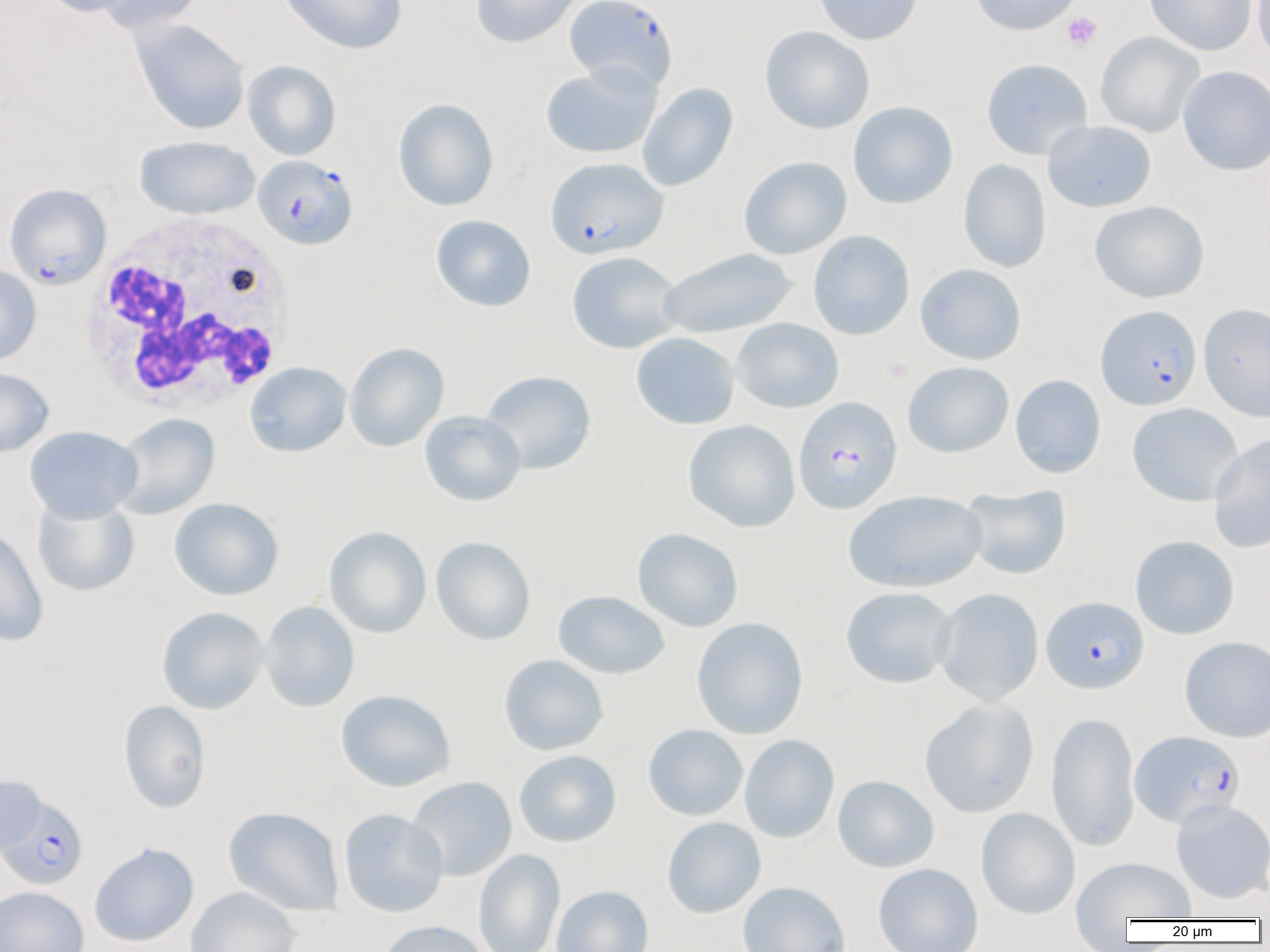

{
  "slide_level_diagnosis": "Plasmodium falciparum",
  "preparation": "thin blood smear",
  "platelet_locations": "approximate bounding boxes as (x1, y1, x2, y2) in pixels: (1063, 12, 1102, 50)",
  "modality": "optical microscopy",
  "white_blood_cell_locations": "approximate bounding boxes as (x1, y1, x2, y2) in pixels: (80, 213, 298, 416)",
  "plasmodium_falciparum_infected_red_blood_cell_locations": "approximate bounding boxes as (x1, y1, x2, y2) in pixels: (565, 0, 677, 92), (253, 155, 357, 249), (545, 157, 668, 259), (4, 183, 111, 290), (1096, 305, 1201, 410), (793, 396, 901, 515), (1041, 596, 1149, 694), (1130, 730, 1244, 828), (0, 794, 89, 890)",
  "image_size": "1270×952 pixels",
  "uninfected_red_blood_cell_locations": "approximate bounding boxes as (x1, y1, x2, y2) in pixels: (43, 0, 142, 18), (94, 0, 205, 35), (278, 0, 407, 55), (469, 0, 585, 49), (813, 0, 923, 45), (968, 0, 1083, 36), (1144, 0, 1257, 55), (1252, 0, 1270, 68), (129, 19, 250, 135), (760, 26, 874, 134), (1095, 31, 1204, 138), (981, 58, 1093, 160), (242, 60, 341, 160), (540, 63, 661, 159), (1178, 65, 1270, 176), (637, 82, 738, 192), (392, 98, 499, 211), (848, 101, 958, 209), (1043, 120, 1157, 212), (133, 135, 260, 220), (738, 155, 852, 259), (958, 159, 1052, 273), (1090, 200, 1210, 303), (430, 214, 536, 312), (808, 230, 915, 340), (658, 248, 797, 338), (566, 251, 684, 354), (915, 263, 1026, 365), (0, 264, 42, 366), (1198, 302, 1270, 421), (732, 318, 844, 413), (631, 332, 740, 429), (344, 341, 449, 452), (902, 361, 1014, 458), (245, 362, 351, 457), (0, 367, 54, 458), (480, 370, 596, 474), (1010, 375, 1106, 478), (1127, 402, 1243, 506), (419, 410, 526, 506), (112, 413, 219, 519), (683, 419, 801, 532), (25, 425, 143, 523), (1208, 433, 1270, 554), (960, 484, 1072, 580), (844, 490, 986, 593), (32, 495, 139, 597), (169, 497, 284, 600), (0, 521, 48, 647), (323, 526, 432, 639), (632, 527, 744, 632), (1130, 535, 1239, 639), (431, 536, 535, 646), (840, 586, 957, 689), (933, 588, 1044, 706), (553, 590, 669, 679), (259, 601, 360, 712), (156, 606, 269, 714), (691, 617, 808, 740), (1180, 635, 1270, 743), (498, 654, 609, 756), (335, 689, 456, 792), (919, 697, 1039, 818), (118, 700, 211, 814), (1046, 711, 1140, 852), (643, 724, 748, 821), (739, 734, 840, 843), (514, 749, 622, 847), (0, 774, 46, 855), (833, 775, 939, 873), (405, 776, 517, 881), (1171, 799, 1270, 904), (223, 806, 344, 917), (339, 808, 448, 917), (976, 808, 1080, 919), (661, 816, 766, 918), (89, 842, 199, 947), (474, 849, 565, 952), (1071, 856, 1195, 923), (873, 863, 984, 952), (737, 882, 850, 952), (551, 885, 653, 952), (0, 886, 89, 952), (186, 886, 300, 952), (377, 920, 491, 952)",
  "field_of_view": "one of a larger specimen",
  "magnification": "1000x"
}